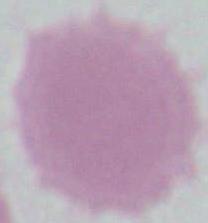

Summary:
  - Magnification: 1000x
  - Identification: erythrocyte
  - Modality: photomicrograph